Locate every blood parasite and identify its species.
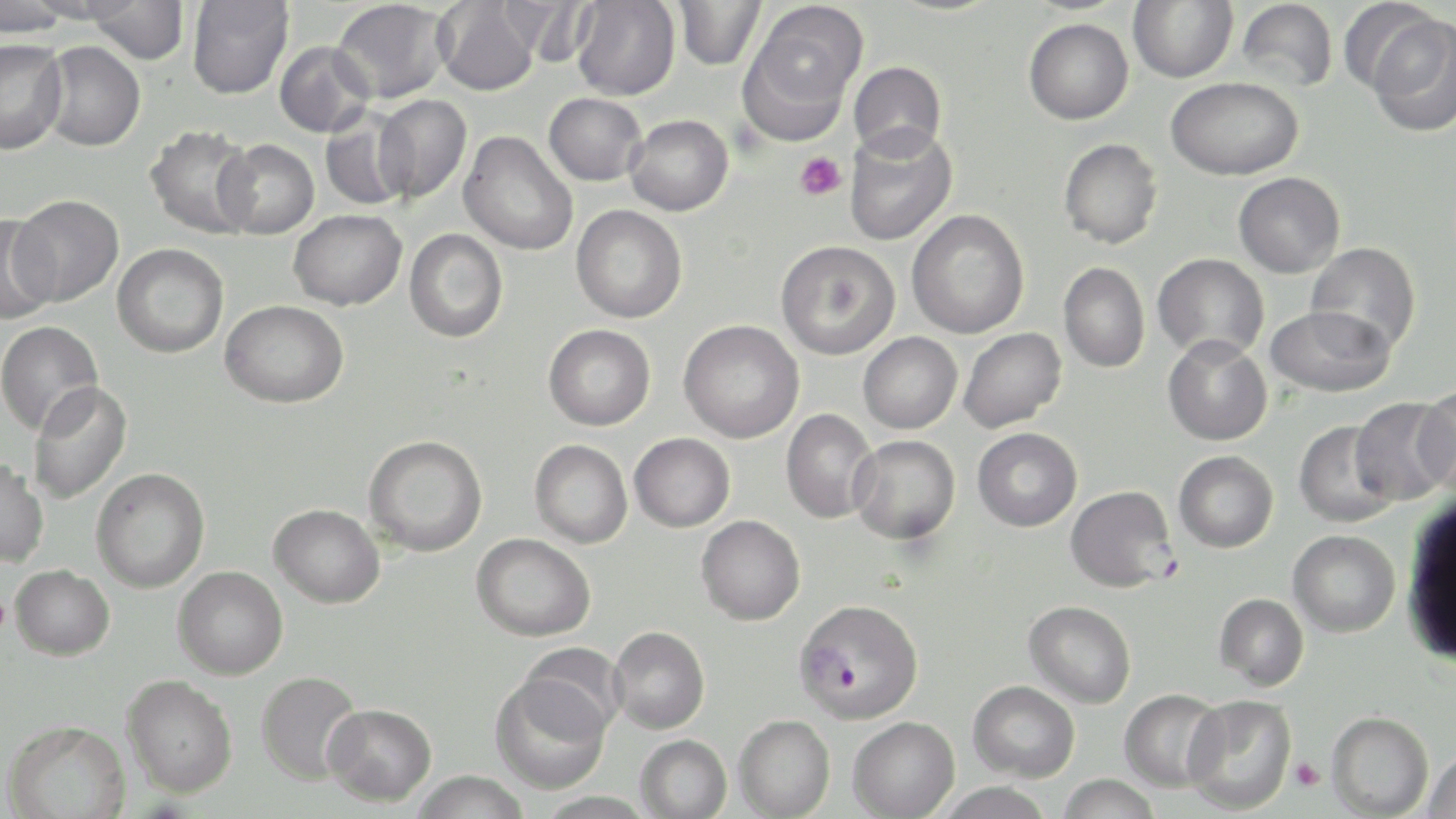
Approximate bounding boxes as (x1,y1)-(x2,y2) corner pairs in pixels.
Plasmodium falciparum-infected red blood cells: (1065,485)-(1178,592), (796,598)-(924,723).
No Plasmodium ovale, Plasmodium malariae, Plasmodium vivax, Babesia divergens, or Trypanosoma brucei observed.

Platelet locations: (794,152)-(845,201), (0,595)-(12,635), (1289,757)-(1326,791). Uninfected red blood cell locations: (0,0)-(73,38), (186,0)-(294,99), (674,0)-(766,70), (1128,0)-(1238,82), (1236,0)-(1338,93), (1337,0)-(1447,96), (330,1)-(452,104), (434,1)-(542,96), (571,1)-(680,100), (84,2)-(190,64), (746,3)-(868,122), (1367,17)-(1456,137), (1023,18)-(1134,124), (0,39)-(68,154), (37,41)-(146,151), (274,41)-(376,138), (848,61)-(947,159), (1165,77)-(1303,180), (543,92)-(647,186), (372,94)-(471,202), (320,108)-(414,212), (625,114)-(734,216), (144,124)-(258,238), (844,125)-(957,246), (459,131)-(579,256), (1058,138)-(1163,249), (215,139)-(320,239), (1233,171)-(1345,278), (10,195)-(124,306), (571,205)-(687,323), (288,209)-(407,311), (906,209)-(1030,339), (0,214)-(60,324), (404,229)-(508,343), (776,240)-(900,359), (1305,242)-(1421,354), (112,243)-(229,357), (1153,252)-(1269,361), (1059,261)-(1150,373), (220,299)-(348,408), (1266,304)-(1396,398), (679,319)-(804,443), (0,320)-(103,436), (543,324)-(656,431), (958,327)-(1066,432), (858,332)-(962,434), (1162,335)-(1272,446), (28,380)-(134,506), (1413,385)-(1456,495), (1351,397)-(1453,505), (781,409)-(879,523), (1293,420)-(1400,528), (972,427)-(1082,532), (629,432)-(735,532), (363,435)-(488,557), (849,435)-(960,544), (530,439)-(633,548), (1173,450)-(1279,552), (0,458)-(49,568), (91,468)-(210,593), (269,503)-(384,609), (696,515)-(805,625), (1287,530)-(1400,638), (471,533)-(596,642), (10,564)-(115,660), (173,566)-(288,679), (1213,593)-(1309,691), (1024,600)-(1136,708), (608,626)-(710,734), (518,642)-(627,737), (256,671)-(363,785), (121,675)-(237,798), (490,675)-(612,795), (968,680)-(1080,782), (1118,688)-(1226,792), (1182,694)-(1297,814), (322,703)-(437,806), (1326,710)-(1434,817), (734,714)-(835,818), (847,716)-(960,819), (3,719)-(130,819), (635,734)-(732,819), (1423,748)-(1456,819), (411,770)-(531,819), (1057,774)-(1162,819), (933,781)-(1056,819), (535,791)-(655,819). Slide-level diagnosis: Plasmodium falciparum. Thin blood smear. Image is 1456×819 pixels. May-Grünwald-Giemsa stain. 1000x magnification. Optical microscopy. Single field of view.